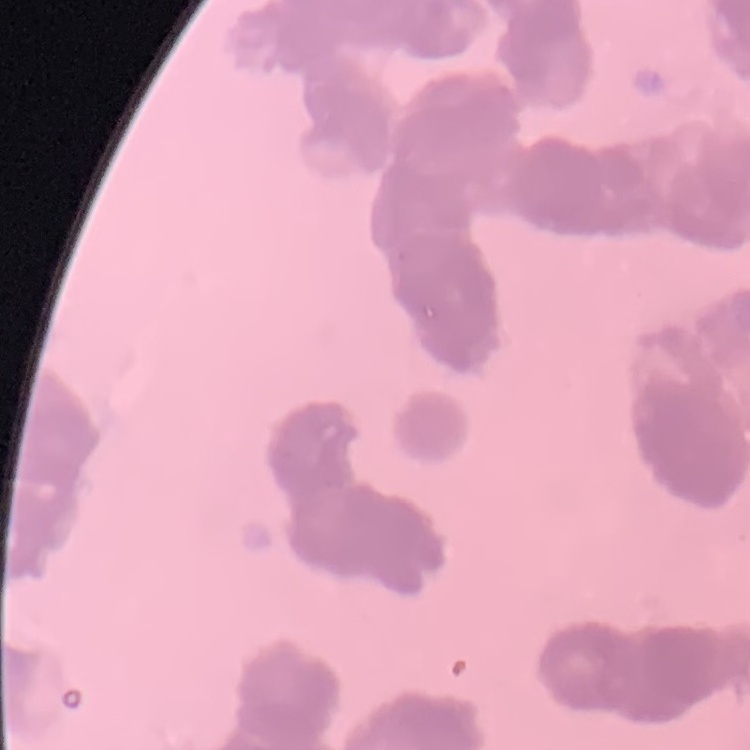
Summary:
  - Erythrocyte morphology: rouleaux formation
  - Stain: Field's or Giemsa
  - Preparation: thin blood film
  - Image type: one tile cut from a larger photomicrograph